Outline each Plasmodium ovale-infected red blood cell.
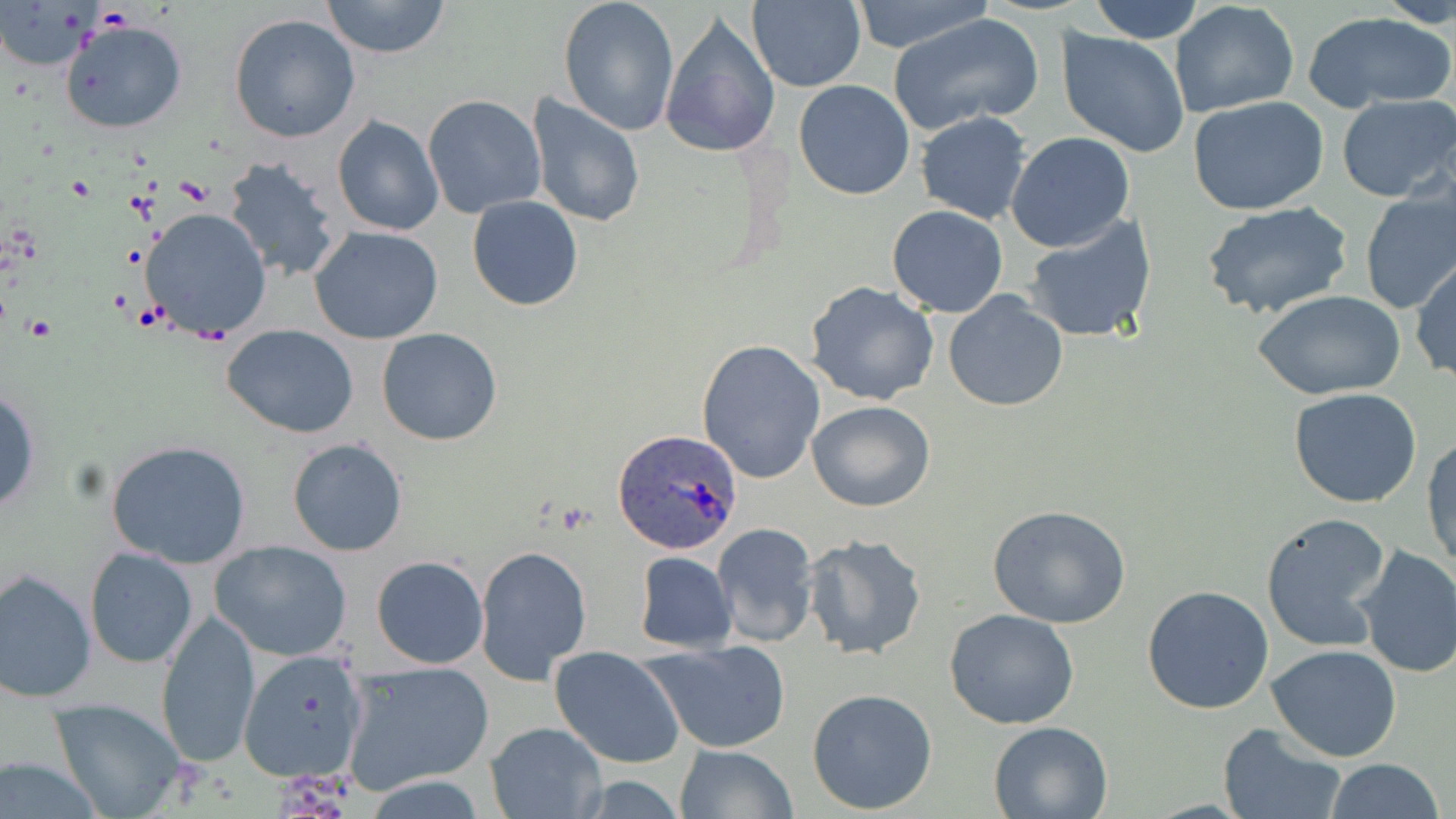

Approximate bounding boxes as (x1, y1, x2, y2) in pixels.
Plasmodium ovale-infected red blood cells: (613, 431, 742, 555).

Uninfected red blood cell locations: (321, 0, 453, 60), (557, 0, 681, 137), (746, 0, 866, 91), (849, 0, 996, 54), (1087, 0, 1206, 43), (1380, 0, 1456, 29), (1169, 1, 1300, 117), (1303, 9, 1455, 113), (888, 11, 1045, 137), (227, 13, 361, 144), (660, 14, 782, 160), (60, 19, 188, 134), (1055, 29, 1190, 160), (793, 80, 917, 200), (526, 94, 646, 229), (1337, 94, 1455, 202), (421, 95, 546, 219), (1188, 96, 1329, 215), (915, 110, 1031, 224), (332, 115, 446, 237), (1006, 131, 1135, 251), (222, 155, 343, 283), (1358, 187, 1456, 315), (467, 196, 583, 311), (1200, 200, 1352, 320), (887, 204, 1008, 318), (140, 207, 272, 343), (1023, 215, 1157, 344), (309, 226, 445, 345), (1411, 256, 1455, 384), (805, 281, 942, 406), (942, 290, 1068, 413), (1256, 290, 1406, 401), (222, 325, 361, 437), (376, 328, 503, 446), (695, 338, 825, 485), (0, 388, 41, 515), (1289, 388, 1423, 509), (806, 399, 935, 512), (1422, 434, 1455, 571), (286, 438, 407, 556), (106, 440, 252, 570), (987, 505, 1134, 628), (1259, 511, 1394, 653), (712, 522, 820, 648), (802, 533, 928, 661), (209, 539, 352, 662), (1352, 544, 1456, 679), (475, 547, 594, 685), (84, 548, 197, 669), (633, 551, 738, 653), (371, 555, 489, 669), (1, 566, 96, 702), (1142, 586, 1275, 715), (943, 609, 1081, 730), (155, 610, 261, 768), (641, 639, 793, 754), (1266, 644, 1402, 761), (238, 646, 372, 785), (550, 646, 685, 769), (340, 659, 496, 796), (806, 687, 938, 814), (47, 698, 188, 818), (987, 719, 1115, 817), (483, 721, 608, 819), (1217, 723, 1348, 819), (674, 744, 799, 819), (1, 753, 108, 818), (1324, 758, 1444, 819). Slide-level diagnosis: Plasmodium ovale. Image is 1456×819 pixels. One field of a larger specimen. May-Grünwald-Giemsa stain. Optical microscopy. Thin blood smear. Captured at 1000x magnification.